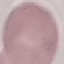
Summary:
  - Malaria status: uninfected
  - Preparation: thin blood smear
  - Capture: smartphone through the microscope eyepiece
  - Stain: Giemsa
  - Image type: cell patch, automatically extracted from a larger field of view and resized to 64 × 64 pixels